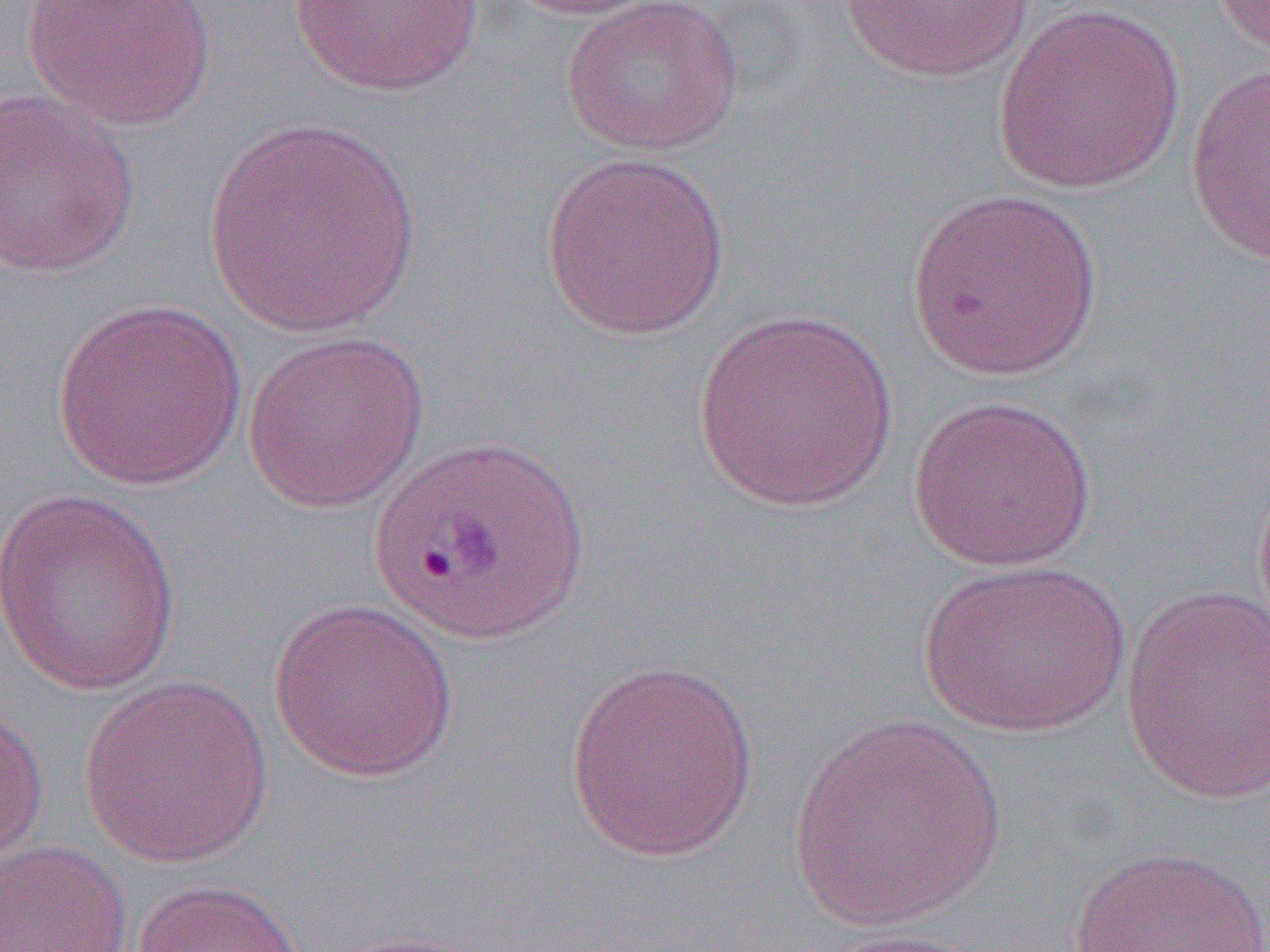

Approximate bounding boxes as named x1/y1/x2/y2 corners in pixels. Uninfected red blood cell locations: (x1=23, y1=0, x2=217, y2=131), (x1=500, y1=0, x2=664, y2=21), (x1=559, y1=0, x2=745, y2=156), (x1=838, y1=0, x2=1037, y2=83), (x1=1208, y1=0, x2=1270, y2=58), (x1=291, y1=1, x2=485, y2=98), (x1=992, y1=3, x2=1187, y2=196), (x1=1185, y1=63, x2=1270, y2=267), (x1=0, y1=88, x2=141, y2=279), (x1=201, y1=116, x2=423, y2=337), (x1=539, y1=151, x2=733, y2=341), (x1=907, y1=187, x2=1104, y2=382), (x1=51, y1=298, x2=249, y2=491), (x1=690, y1=308, x2=901, y2=514), (x1=241, y1=330, x2=431, y2=514), (x1=906, y1=394, x2=1099, y2=573), (x1=1253, y1=470, x2=1270, y2=644), (x1=0, y1=488, x2=182, y2=695), (x1=916, y1=559, x2=1132, y2=738), (x1=1120, y1=584, x2=1270, y2=807), (x1=267, y1=597, x2=460, y2=783), (x1=564, y1=658, x2=759, y2=863), (x1=78, y1=673, x2=275, y2=868), (x1=0, y1=697, x2=50, y2=871), (x1=785, y1=713, x2=1010, y2=931), (x1=0, y1=840, x2=133, y2=951), (x1=1063, y1=846, x2=1270, y2=952), (x1=131, y1=878, x2=305, y2=952), (x1=810, y1=927, x2=992, y2=952). Slide-level diagnosis: Plasmodium ovale. Thin blood smear. Captured at 1000x magnification. One field of a larger specimen. Light microscopy. Image is 1270×952 pixels.